State which parasite is depicted.
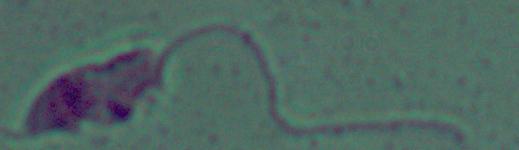
Leishmania.

magnification = 1000x
modality = photomicrograph